Name the parasite shown.
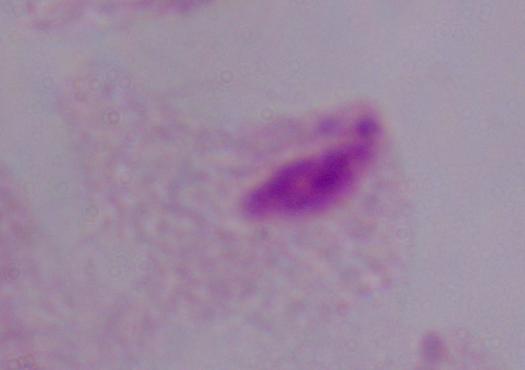

A trichomonad.

magnification: 1000x
modality: photomicrograph